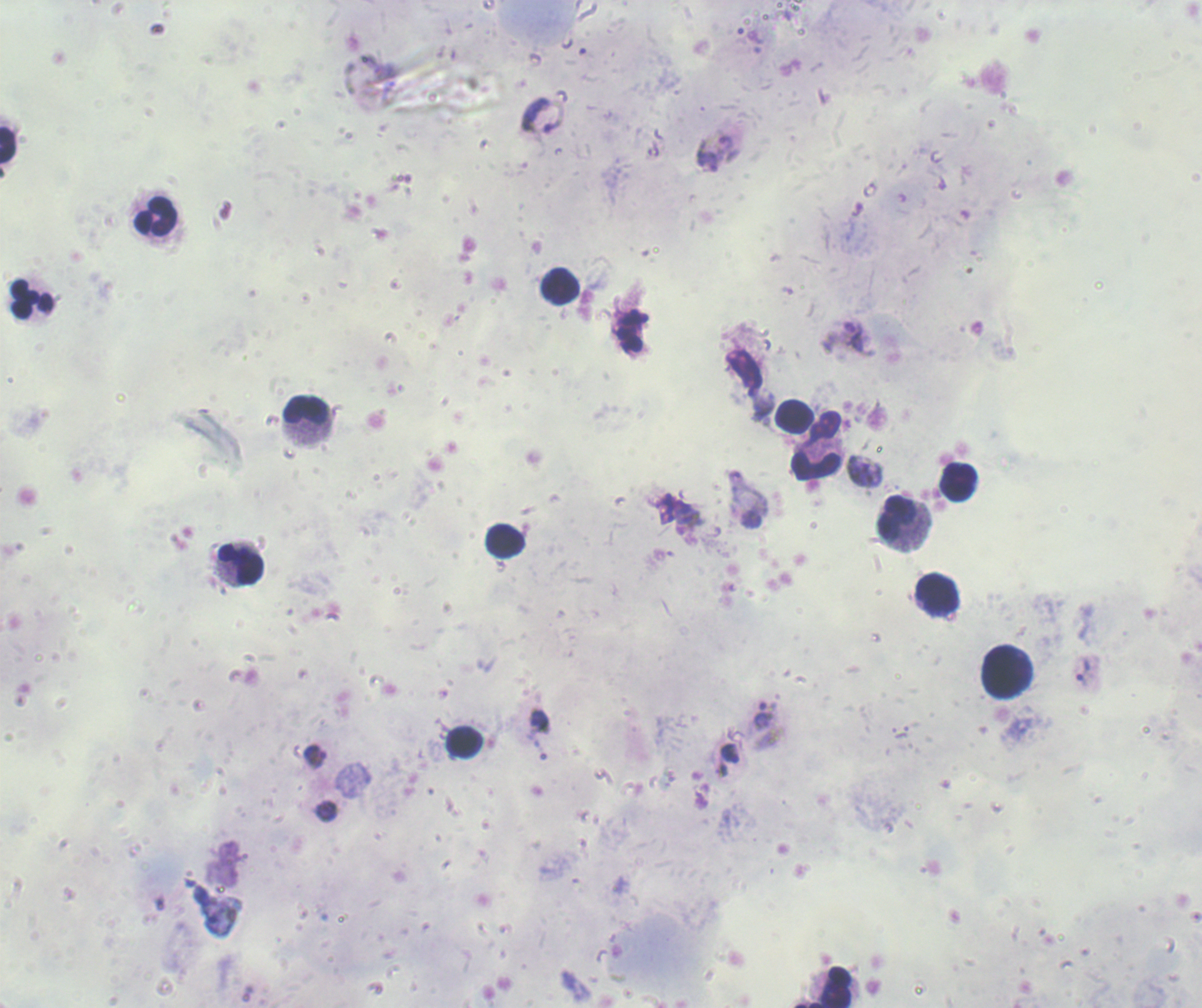

Approximate centers as {x, y} in pixels. Trophozoite locations: {538, 117}, {726, 143}, {708, 163}, {865, 471}, {664, 508}, {687, 513}, {1082, 671}, {762, 714}, {539, 721}, {730, 753}, {315, 754}, {326, 811}. Leukocyte locations: {7, 144}, {156, 216}, {559, 286}, {32, 297}, {305, 415}, {794, 415}, {816, 459}, {957, 482}, {902, 520}, {505, 540}, {236, 567}, {938, 595}, {1005, 670}, {464, 741}, {826, 987}. Background quality: unsatisfactory. Romanowsky stain. 100x magnification. Result: Plasmodium parasites identified. Image is 1202×1008 pixels. Thick smear of blood. One field from this slide. Previously used in a real diagnosis.